Locate every Plasmodium parasite.
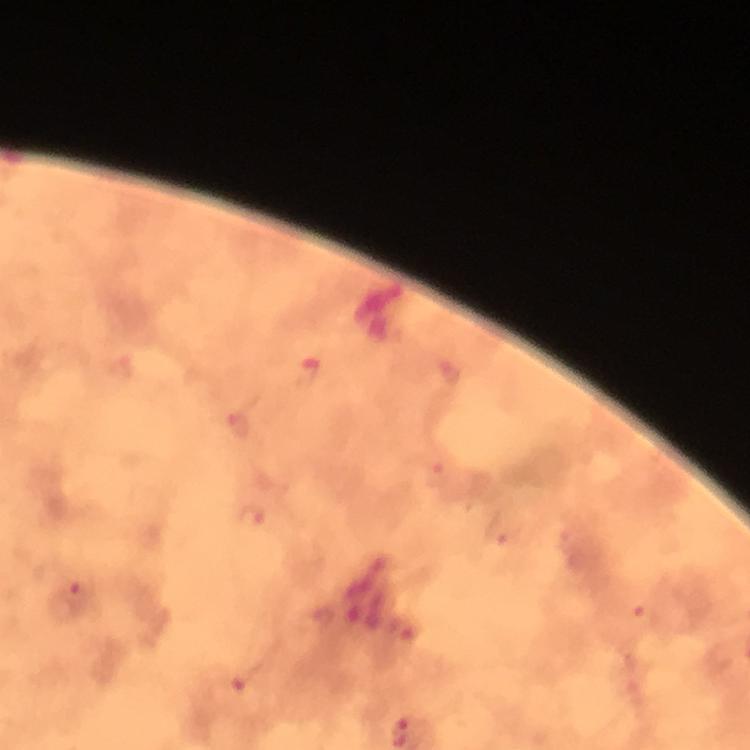

Approximate centers as (x, y) in pixels.
Plasmodium parasites: (308, 370), (450, 373), (237, 424), (437, 474), (251, 517), (506, 528), (78, 590), (644, 617), (404, 629), (246, 677).

context = from a malaria diagnostic workup
preparation = thick blood smear
image size = 750×750 pixels
cropped from = one field of view
magnification = 100x
stain = Giemsa
immersion oil = applied
capture = smartphone mounted on the microscope